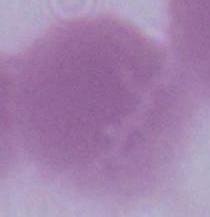

A red blood cell is shown. Captured at 1000x magnification. Micrograph.